Describe the morphology of the red blood cells.
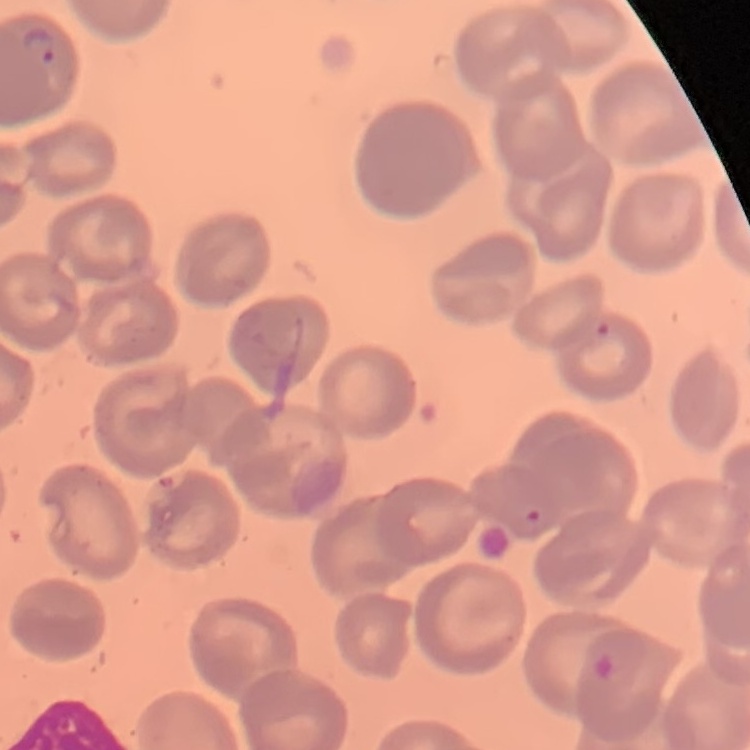

No rouleaux formation.

preparation: thin blood smear
stain: Field's or Giemsa
image_type: square crop of a larger photomicrograph